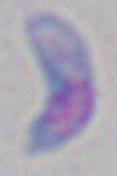

Summary:
  - Identification: Toxoplasma gondii
  - Modality: micrograph
  - Magnification: 1000x